Name the parasite shown.
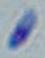

Toxoplasma gondii.

Summary:
  - Magnification: 1000x
  - Modality: micrograph